Assess the morphology of the red blood cells.
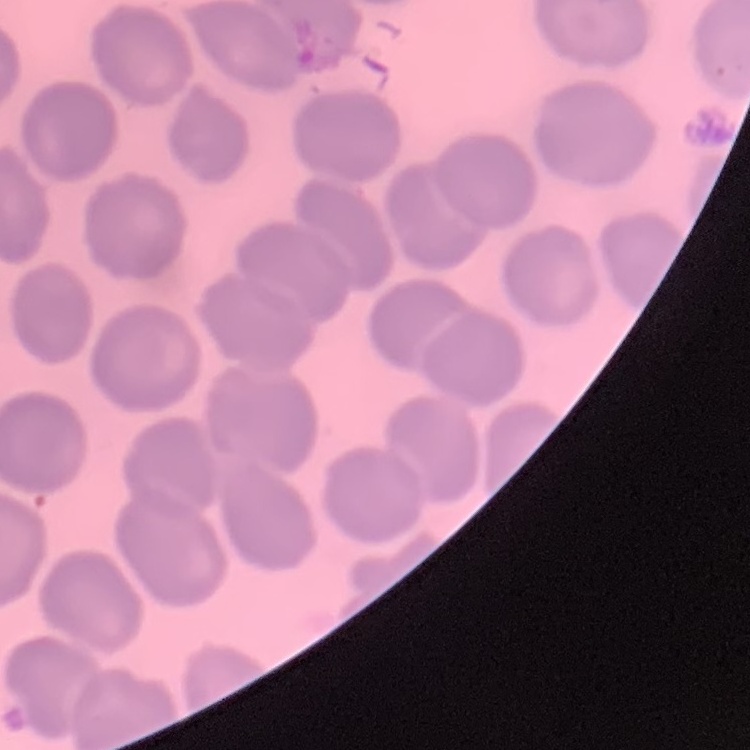
They show no rouleaux formation.

preparation = thin blood film
image type = square crop of a larger photomicrograph
stain = Field's or Giemsa